Locate every P. falciparum parasite and identify its life-cycle stage.
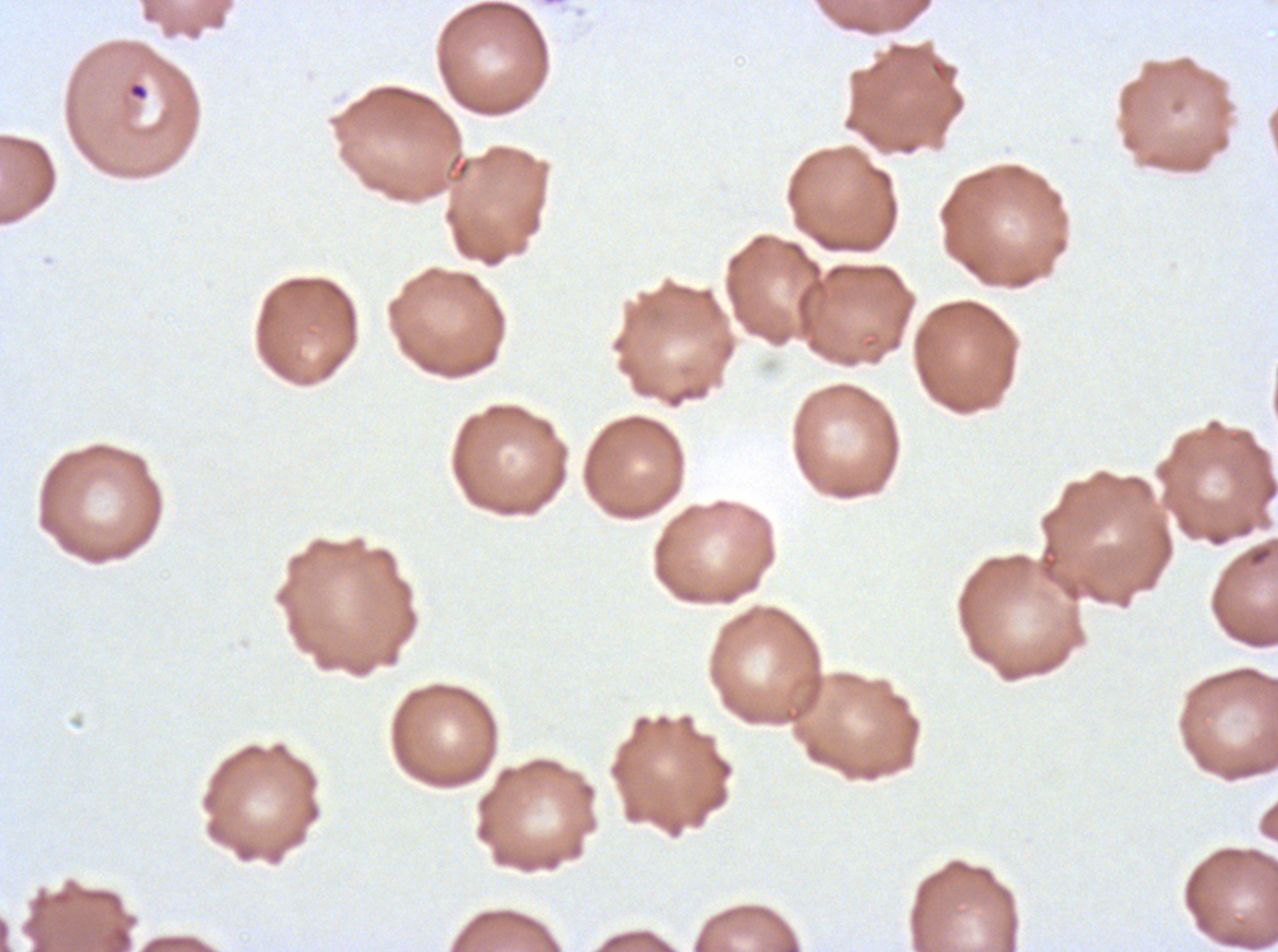
Approximate bounding boxes as (x1, y1, x2, y2) in pixels.
Rings: (128, 81, 149, 101).
No late-ring/early-trophozoite forms, mid trophozoites, late trophozoites, early schizonts, late schizonts, segmenters, or gametocytes observed.

Ex-vivo P. falciparum culture from a patient in The Gambia, grown for 24 to 48 hours. Giemsa-stained preparation. Image is 1278×952 pixels. Thin blood smear. A sub-image separated from a larger composite.